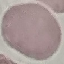
Summary:
  - Malaria status: uninfected
  - Image type: cell patch, automatically extracted from a larger field of view and resized to 64 × 64 pixels
  - Preparation: thin blood film
  - Capture: smartphone camera at the microscope eyepiece
  - Stain: Giemsa